Report the malaria status of this cell.
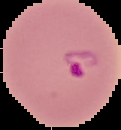
Parasitized.

Summary:
  - Preparation: thin blood film
  - Image type: cell region segmented out of the field of view; surrounding area masked to black
  - Image size: 121×130 pixels